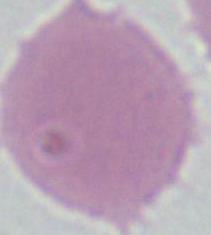
magnification: 1000x
identification: erythrocyte
modality: micrograph